Name the parasite shown.
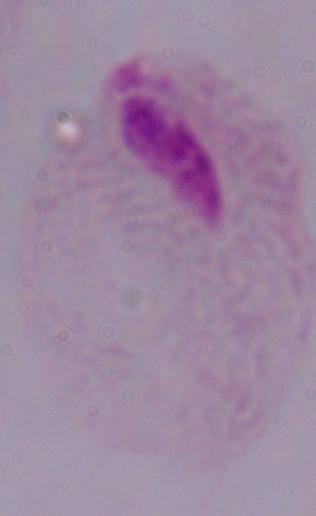

A trichomonad.

Summary:
  - Magnification: 1000x
  - Modality: micrograph